Point out each Plasmodium parasite.
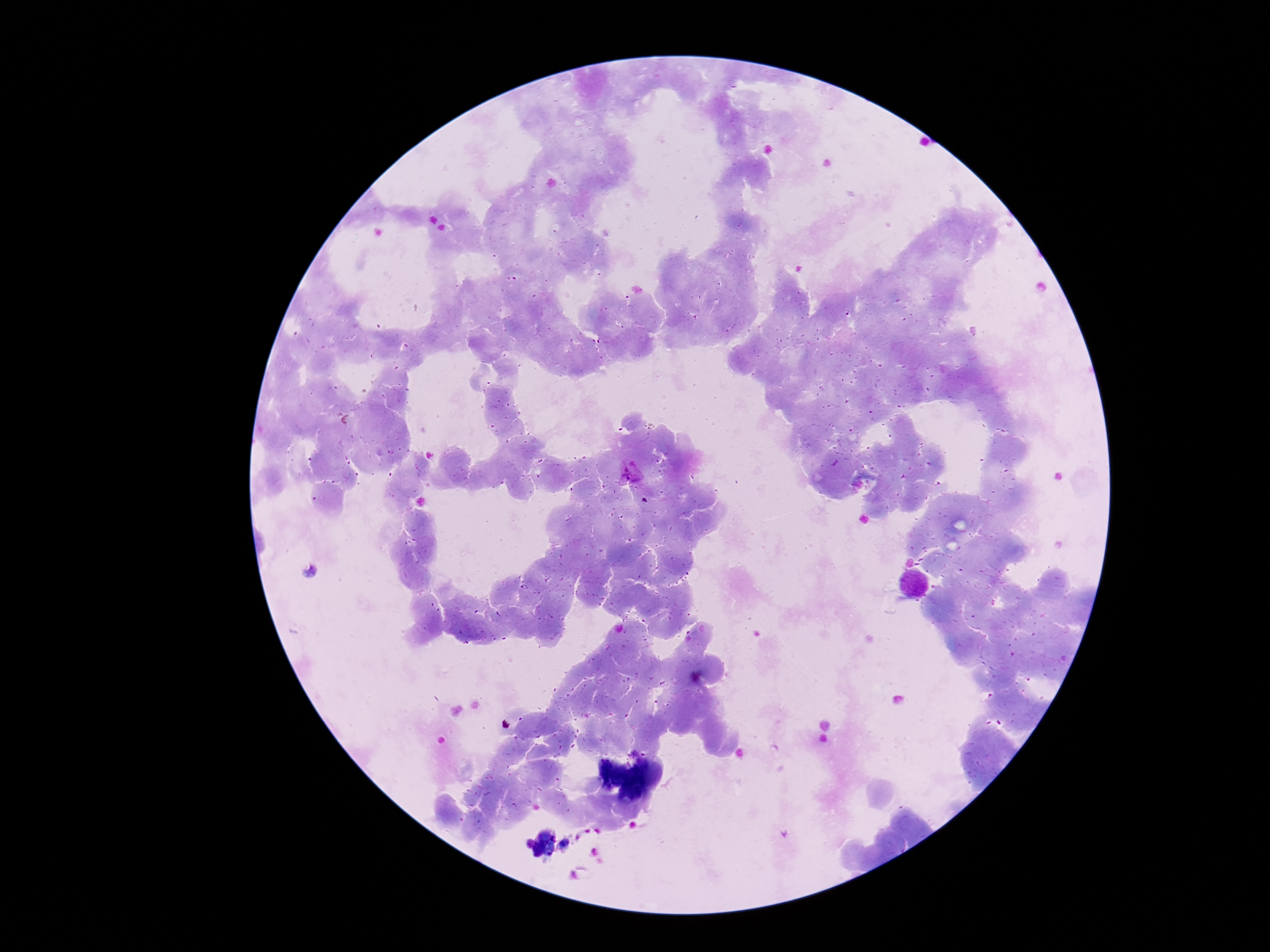

Approximate object centers, in pixels from the top-left corner.
Plasmodium parasites: (x=630, y=475).

field of view = one from this slide
stain = Giemsa
patient malaria status = positive
capture = smartphone camera through the microscope eyepiece
magnification = 100x
image size = 1270×952 pixels
preparation = thick blood smear